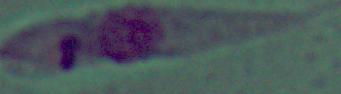
magnification = 1000x
identification = Leishmania
modality = micrograph